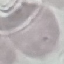

Malaria status: uninfected. Photographed with a smartphone camera at the microscope eyepiece. Giemsa-stained preparation. Thin blood film. Automatically extracted cell patch, resized to 64 × 64 pixels.